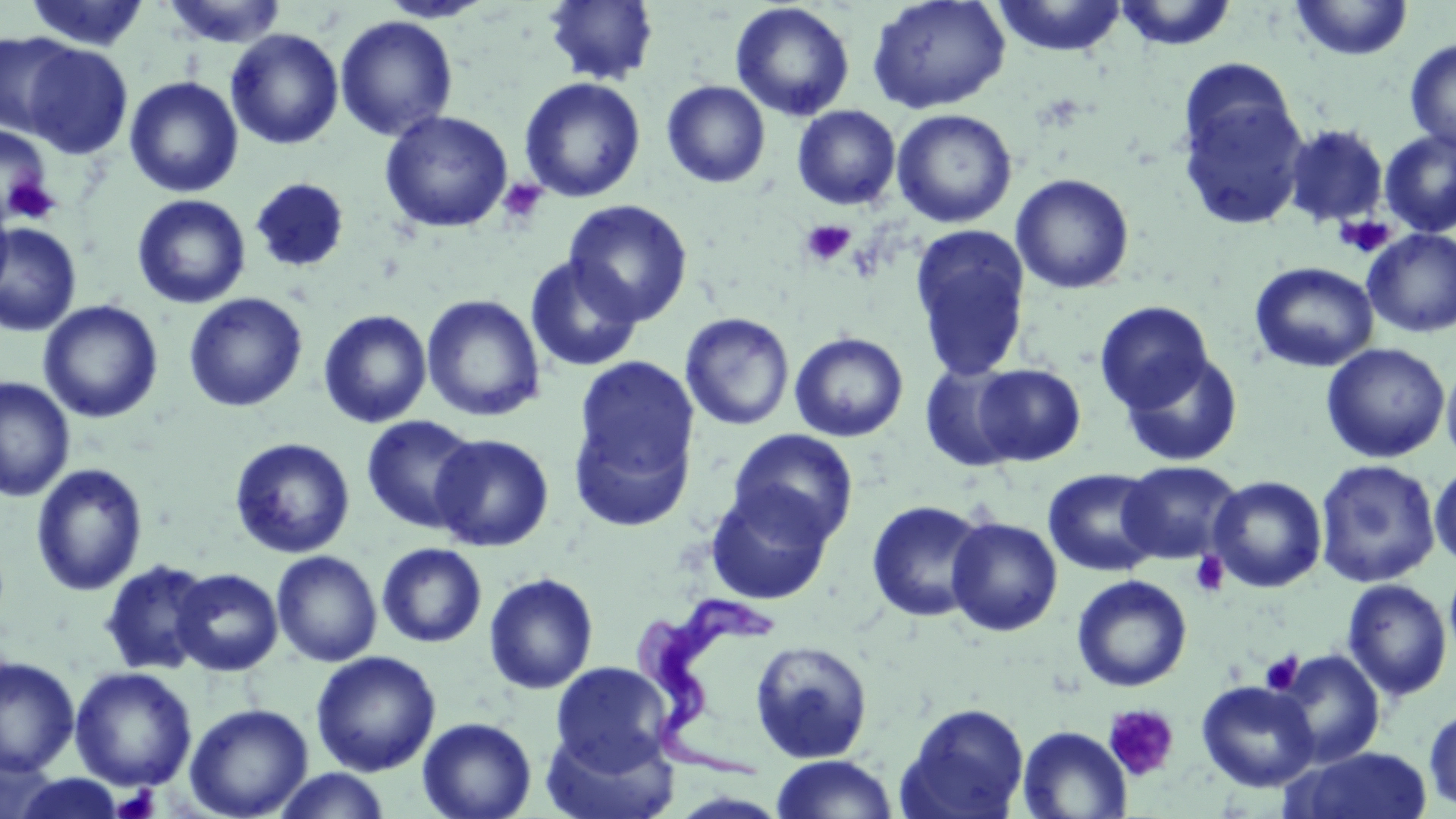 Approximate bounding boxes as named x1/y1/x2/y2 corners in pixels. Trypanosoma brucei locations: (x1=634, y1=591, x2=781, y2=781). Uninfected red blood cell locations: (x1=24, y1=0, x2=150, y2=51), (x1=378, y1=0, x2=495, y2=23), (x1=544, y1=0, x2=659, y2=86), (x1=867, y1=0, x2=1011, y2=113), (x1=992, y1=0, x2=1128, y2=58), (x1=1291, y1=0, x2=1413, y2=61), (x1=160, y1=1, x2=288, y2=48), (x1=1113, y1=1, x2=1238, y2=51), (x1=730, y1=2, x2=855, y2=121), (x1=335, y1=16, x2=458, y2=141), (x1=226, y1=28, x2=344, y2=150), (x1=0, y1=31, x2=77, y2=138), (x1=1404, y1=38, x2=1456, y2=153), (x1=22, y1=43, x2=133, y2=158), (x1=124, y1=76, x2=243, y2=197), (x1=519, y1=77, x2=646, y2=203), (x1=661, y1=80, x2=771, y2=188), (x1=1177, y1=82, x2=1310, y2=232), (x1=792, y1=105, x2=901, y2=210), (x1=891, y1=108, x2=1017, y2=228), (x1=380, y1=110, x2=514, y2=233), (x1=0, y1=123, x2=55, y2=226), (x1=1282, y1=123, x2=1389, y2=228), (x1=1379, y1=129, x2=1456, y2=238), (x1=1011, y1=173, x2=1134, y2=295), (x1=251, y1=177, x2=350, y2=273), (x1=132, y1=194, x2=251, y2=309), (x1=0, y1=196, x2=14, y2=302), (x1=563, y1=200, x2=694, y2=326), (x1=0, y1=222, x2=82, y2=337), (x1=910, y1=226, x2=1032, y2=381), (x1=1363, y1=229, x2=1456, y2=338), (x1=524, y1=254, x2=644, y2=373), (x1=1249, y1=261, x2=1378, y2=372), (x1=184, y1=293, x2=308, y2=412), (x1=422, y1=294, x2=546, y2=422), (x1=39, y1=299, x2=163, y2=424), (x1=1095, y1=301, x2=1215, y2=415), (x1=318, y1=309, x2=433, y2=428), (x1=680, y1=312, x2=795, y2=431), (x1=790, y1=332, x2=909, y2=442), (x1=1321, y1=343, x2=1451, y2=463), (x1=1120, y1=352, x2=1243, y2=467), (x1=570, y1=355, x2=700, y2=523), (x1=1441, y1=360, x2=1456, y2=467), (x1=920, y1=361, x2=1028, y2=473), (x1=972, y1=363, x2=1086, y2=466), (x1=0, y1=376, x2=75, y2=502), (x1=361, y1=415, x2=481, y2=534), (x1=728, y1=428, x2=859, y2=546), (x1=431, y1=433, x2=555, y2=552), (x1=229, y1=437, x2=356, y2=559), (x1=1315, y1=459, x2=1441, y2=587), (x1=1118, y1=460, x2=1243, y2=565), (x1=30, y1=463, x2=148, y2=596), (x1=1429, y1=463, x2=1456, y2=570), (x1=1042, y1=468, x2=1162, y2=577), (x1=1207, y1=475, x2=1327, y2=593), (x1=705, y1=485, x2=835, y2=605), (x1=866, y1=499, x2=990, y2=623), (x1=946, y1=518, x2=1063, y2=637), (x1=376, y1=542, x2=487, y2=648), (x1=271, y1=550, x2=382, y2=667), (x1=98, y1=558, x2=216, y2=676), (x1=171, y1=567, x2=284, y2=676), (x1=483, y1=572, x2=599, y2=694), (x1=1072, y1=574, x2=1192, y2=692), (x1=1341, y1=578, x2=1453, y2=701), (x1=749, y1=639, x2=874, y2=764), (x1=1275, y1=649, x2=1385, y2=767), (x1=311, y1=650, x2=441, y2=777), (x1=0, y1=656, x2=80, y2=777), (x1=551, y1=661, x2=673, y2=772), (x1=69, y1=666, x2=198, y2=791), (x1=1196, y1=679, x2=1320, y2=792), (x1=184, y1=702, x2=314, y2=819), (x1=898, y1=703, x2=1031, y2=819), (x1=1423, y1=705, x2=1456, y2=813), (x1=417, y1=717, x2=537, y2=819), (x1=1016, y1=725, x2=1132, y2=819), (x1=541, y1=726, x2=679, y2=819), (x1=1285, y1=745, x2=1435, y2=818), (x1=0, y1=747, x2=59, y2=818), (x1=770, y1=754, x2=898, y2=818), (x1=271, y1=768, x2=394, y2=819), (x1=11, y1=774, x2=128, y2=818). Platelet locations: (x1=497, y1=178, x2=548, y2=225), (x1=3, y1=179, x2=62, y2=225), (x1=1334, y1=214, x2=1397, y2=259), (x1=799, y1=219, x2=856, y2=267), (x1=1189, y1=551, x2=1230, y2=598), (x1=1260, y1=652, x2=1303, y2=695), (x1=1103, y1=704, x2=1179, y2=782), (x1=111, y1=784, x2=160, y2=818). Slide-level diagnosis: Trypanosoma brucei. Single field of view. Image is 1456×819 pixels. Captured at 1000x magnification. Thin blood film. Light microscopy. May-Grünwald-Giemsa stain.